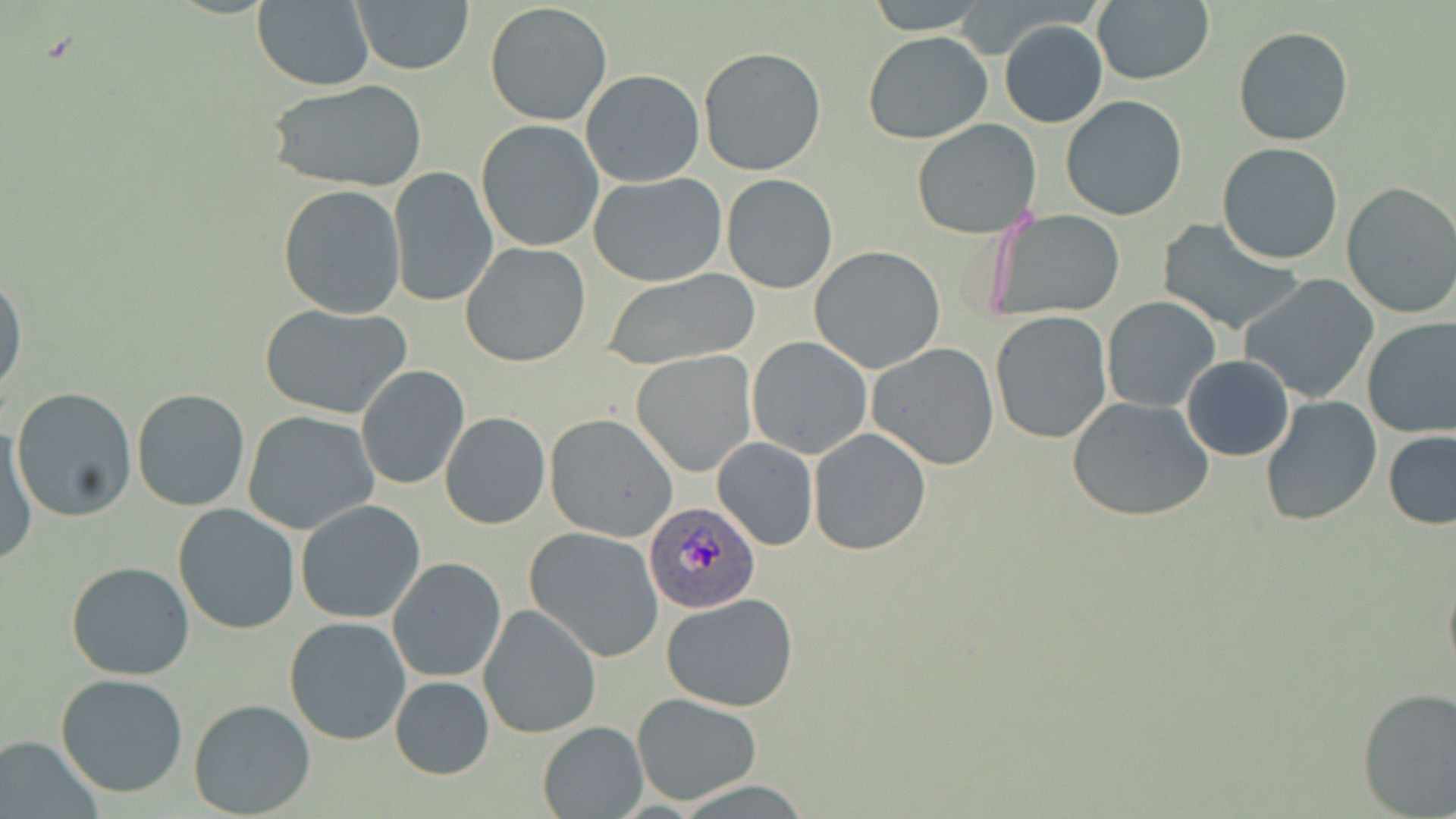

slide-level diagnosis = Plasmodium ovale
magnification = 1000x
modality = optical microscopy
field of view = one of a larger specimen
image size = 1456×819 pixels
preparation = thin blood film
uninfected red blood cell locations = approximate bounding boxes as (x1,y1)-(x2,y2) corner pairs in pixels: (865,0)-(988,33), (1091,0)-(1215,85), (250,1)-(375,90), (351,2)-(474,75), (485,2)-(612,126), (999,19)-(1109,128), (1234,27)-(1353,146), (864,30)-(994,144), (697,46)-(826,178), (581,69)-(703,186), (266,77)-(427,193), (1059,95)-(1188,222), (475,119)-(606,254), (912,119)-(1043,239), (1217,142)-(1345,265), (388,167)-(498,308), (589,173)-(728,286), (721,174)-(837,293), (1339,181)-(1456,321), (278,184)-(406,320), (987,210)-(1124,319), (1156,220)-(1305,336), (462,243)-(590,368), (809,247)-(947,373), (0,267)-(26,406), (601,268)-(760,369), (1238,274)-(1382,405), (1101,295)-(1221,413), (259,303)-(412,420), (989,311)-(1112,445), (1362,318)-(1456,440), (747,336)-(872,459), (867,342)-(1000,469), (632,351)-(756,477), (1182,355)-(1294,460), (354,364)-(469,489), (11,388)-(137,522), (131,389)-(252,512), (1259,395)-(1383,525), (1067,396)-(1215,522), (242,410)-(381,536), (440,411)-(550,529), (543,413)-(678,541), (1,420)-(36,568), (807,428)-(931,555), (1383,428)-(1456,530), (713,438)-(819,551), (295,500)-(426,624), (172,503)-(302,634), (524,526)-(665,661), (388,557)-(506,682), (66,561)-(196,681), (1442,562)-(1456,687), (661,593)-(801,712), (477,603)-(601,740), (284,616)-(412,746), (55,672)-(189,797), (390,675)-(493,779), (1356,687)-(1456,817), (630,694)-(765,805), (188,697)-(316,818), (538,720)-(647,818), (1,734)-(104,818)
stain = May-Grünwald-Giemsa
Plasmodium ovale-infected red blood cell locations = approximate bounding boxes as (x1,y1)-(x2,y2) corner pairs in pixels: (642,499)-(758,614)